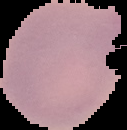
Image is 127×130 pixels. Cell region segmented out of the field of view; the surrounding area is masked to black. Result: negative for Plasmodium parasites. From a thin blood film.